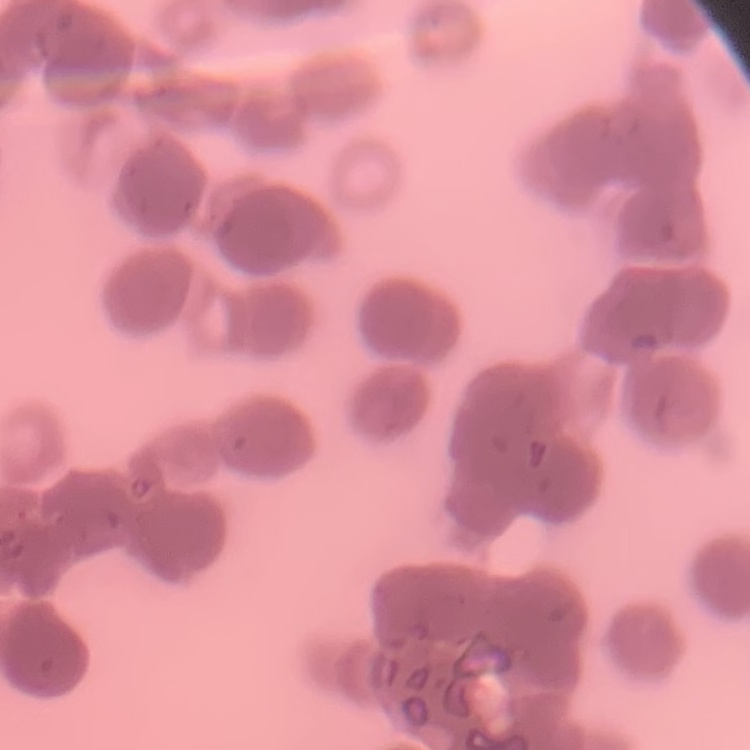

Summary:
  - Erythrocyte morphology: rouleaux formation
  - Preparation: thin blood smear
  - Stain: Field's or Giemsa
  - Image type: square crop of a larger photomicrograph